Give the position of every leukocyte visible.
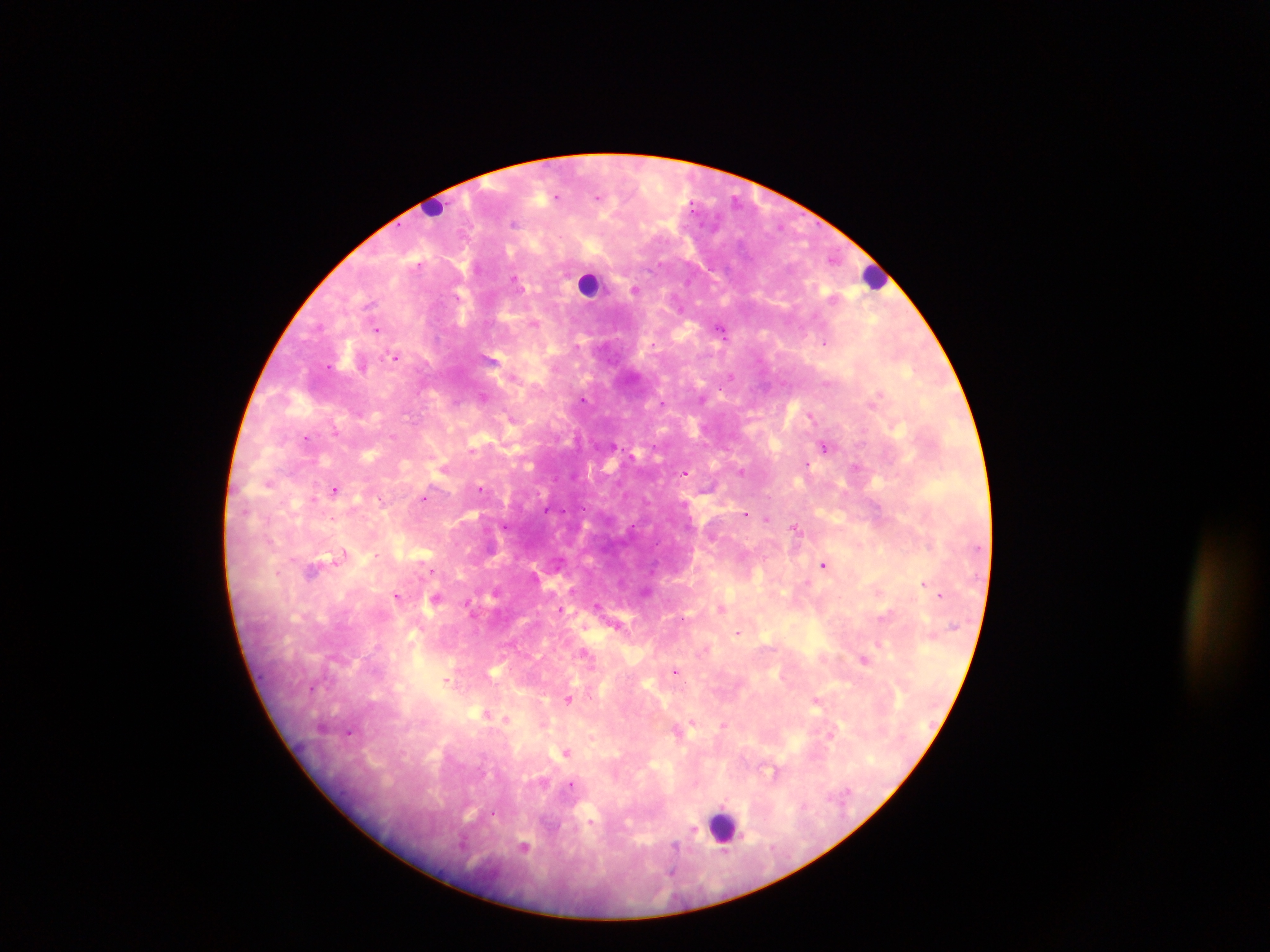

Approximate centers as (x, y) in pixels.
Leukocytes: (432, 207), (874, 275), (590, 283), (723, 826).

field of view = single
image size = 1270×952 pixels
country = Ghana
capture = mobile-phone photograph through a microscope
preparation = thick blood smear
Plasmodium parasite locations = approximate centers as (x, y) in pixels: (599, 195), (736, 200), (515, 278), (636, 289), (534, 322), (722, 328), (377, 329), (825, 343), (396, 356), (876, 395), (483, 397), (582, 400), (662, 402), (811, 415), (513, 417), (337, 431), (306, 437), (824, 445), (471, 449), (445, 469), (742, 470), (686, 472), (270, 481), (481, 487), (335, 489), (424, 498), (313, 499), (746, 513), (766, 518), (505, 526), (796, 528), (341, 556), (824, 565), (924, 582), (878, 590), (496, 591), (646, 591), (397, 594), (940, 595), (437, 597), (468, 603), (722, 607), (561, 608), (618, 625), (737, 633), (879, 645), (585, 652), (864, 660), (677, 671), (447, 679), (313, 687), (569, 698), (816, 701), (487, 713), (506, 719), (693, 721), (724, 725), (350, 732), (830, 733), (568, 752), (776, 773), (571, 784), (524, 846)